Assess the morphology of the erythrocytes.
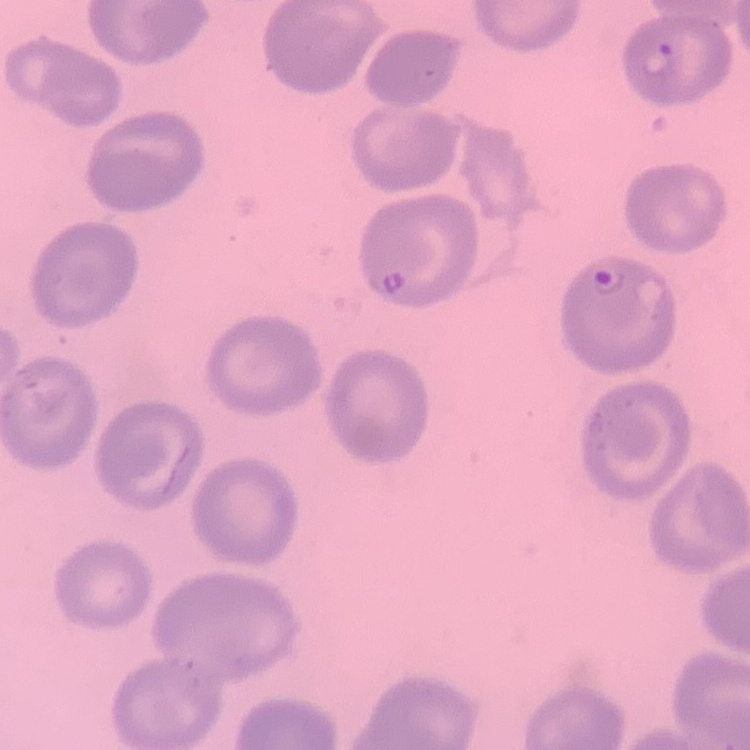
No rouleaux formation.

Summary:
  - Stain: Field's or Giemsa
  - Preparation: thin blood film
  - Image type: one tile cut from a larger photomicrograph